Locate every Plasmodium falciparum-infected red blood cell.
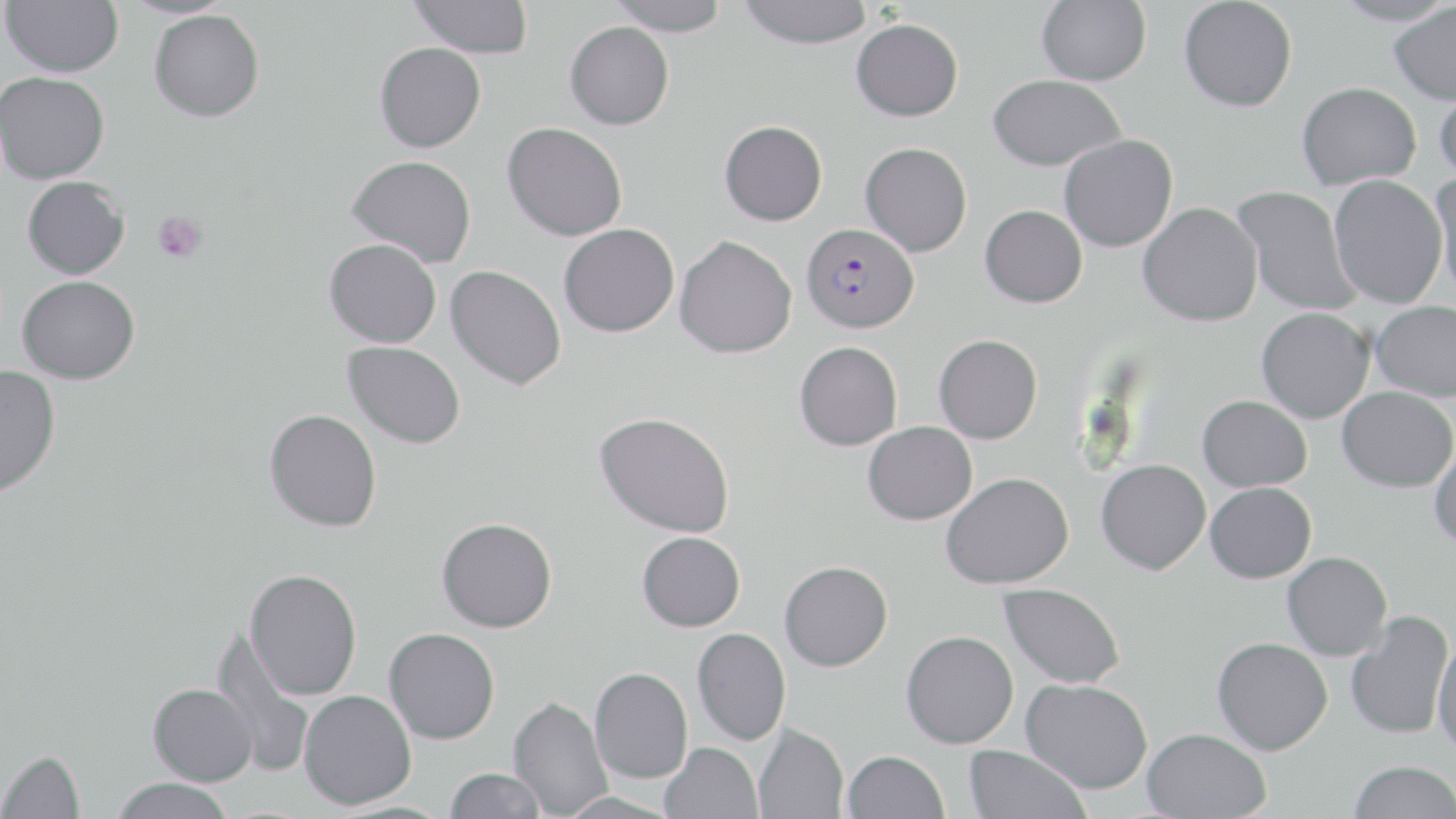

Approximate bounding boxes as named x1/y1/x2/y2 corners in pixels.
Plasmodium falciparum-infected red blood cells: (x1=801, y1=222, x2=919, y2=333).

slide-level diagnosis = Plasmodium falciparum
stain = May-Grünwald-Giemsa
magnification = 1000x
preparation = thin blood film
uninfected red blood cell locations = approximate bounding boxes as named x1/y1/x2/y2 corners in pixels: (x1=2, y1=0, x2=124, y2=78), (x1=410, y1=0, x2=533, y2=58), (x1=607, y1=0, x2=732, y2=36), (x1=738, y1=0, x2=874, y2=49), (x1=1037, y1=0, x2=1151, y2=85), (x1=1178, y1=0, x2=1297, y2=112), (x1=1331, y1=0, x2=1456, y2=27), (x1=1388, y1=4, x2=1456, y2=104), (x1=149, y1=9, x2=265, y2=122), (x1=851, y1=18, x2=963, y2=121), (x1=564, y1=21, x2=674, y2=130), (x1=374, y1=42, x2=486, y2=153), (x1=0, y1=71, x2=110, y2=184), (x1=988, y1=74, x2=1126, y2=171), (x1=1296, y1=82, x2=1421, y2=190), (x1=1434, y1=85, x2=1456, y2=187), (x1=719, y1=120, x2=827, y2=225), (x1=502, y1=122, x2=627, y2=241), (x1=1059, y1=135, x2=1178, y2=252), (x1=860, y1=142, x2=972, y2=256), (x1=347, y1=155, x2=476, y2=268), (x1=1430, y1=171, x2=1456, y2=299), (x1=1328, y1=175, x2=1447, y2=308), (x1=22, y1=176, x2=130, y2=279), (x1=1232, y1=185, x2=1360, y2=317), (x1=1138, y1=202, x2=1263, y2=327), (x1=980, y1=204, x2=1087, y2=307), (x1=559, y1=223, x2=679, y2=337), (x1=674, y1=235, x2=797, y2=358), (x1=324, y1=238, x2=442, y2=347), (x1=445, y1=265, x2=566, y2=390), (x1=17, y1=275, x2=140, y2=384), (x1=1371, y1=300, x2=1456, y2=400), (x1=1256, y1=308, x2=1374, y2=423), (x1=934, y1=334, x2=1042, y2=443), (x1=343, y1=341, x2=466, y2=448), (x1=794, y1=341, x2=903, y2=451), (x1=0, y1=365, x2=60, y2=498), (x1=1337, y1=386, x2=1456, y2=492), (x1=1197, y1=395, x2=1312, y2=491), (x1=264, y1=409, x2=382, y2=531), (x1=595, y1=412, x2=735, y2=537), (x1=863, y1=421, x2=977, y2=525), (x1=1430, y1=441, x2=1456, y2=550), (x1=1096, y1=459, x2=1210, y2=575), (x1=940, y1=473, x2=1075, y2=589), (x1=1205, y1=482, x2=1316, y2=582), (x1=437, y1=517, x2=557, y2=632), (x1=637, y1=531, x2=745, y2=631), (x1=1282, y1=551, x2=1392, y2=660), (x1=779, y1=560, x2=893, y2=671), (x1=244, y1=569, x2=362, y2=700), (x1=999, y1=582, x2=1125, y2=688), (x1=1345, y1=610, x2=1453, y2=741), (x1=692, y1=627, x2=791, y2=745), (x1=383, y1=628, x2=500, y2=744), (x1=901, y1=630, x2=1018, y2=748), (x1=212, y1=634, x2=316, y2=778), (x1=1432, y1=634, x2=1456, y2=757), (x1=1211, y1=637, x2=1333, y2=754), (x1=589, y1=667, x2=693, y2=783), (x1=1021, y1=678, x2=1153, y2=793), (x1=148, y1=683, x2=258, y2=787), (x1=299, y1=690, x2=416, y2=809), (x1=508, y1=696, x2=612, y2=818), (x1=753, y1=723, x2=848, y2=819), (x1=1142, y1=728, x2=1271, y2=818), (x1=660, y1=742, x2=763, y2=819), (x1=963, y1=744, x2=1091, y2=819), (x1=0, y1=749, x2=85, y2=819), (x1=842, y1=749, x2=949, y2=819), (x1=1349, y1=760, x2=1456, y2=819), (x1=444, y1=767, x2=546, y2=819), (x1=109, y1=777, x2=236, y2=819), (x1=556, y1=791, x2=681, y2=819)
modality = optical microscopy
image size = 1456×819 pixels
platelet locations = approximate bounding boxes as named x1/y1/x2/y2 corners in pixels: (x1=151, y1=210, x2=208, y2=263)
field of view = single